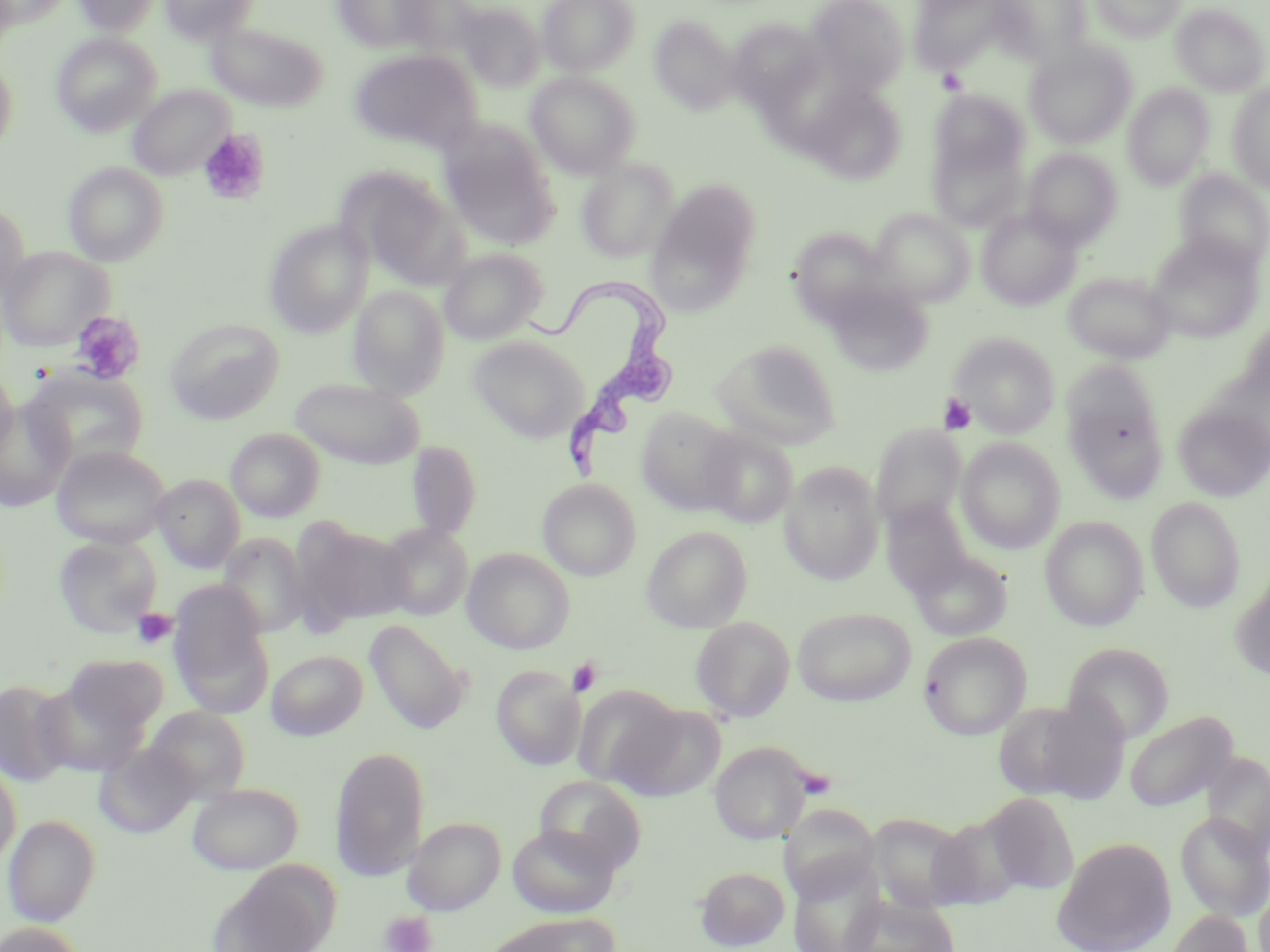
Approximate bounding boxes as [x1, y1, x2, y2] in pixels. Uninfected red blood cell locations: [73, 0, 162, 36], [158, 0, 261, 44], [333, 0, 436, 53], [537, 0, 640, 75], [805, 0, 909, 95], [909, 0, 1009, 73], [987, 0, 1092, 63], [1090, 0, 1185, 42], [393, 1, 481, 56], [454, 2, 547, 91], [1171, 3, 1269, 96], [649, 15, 739, 114], [728, 19, 828, 111], [206, 22, 328, 112], [52, 32, 161, 136], [1024, 41, 1137, 148], [349, 49, 482, 155], [0, 54, 18, 157], [526, 72, 640, 178], [805, 82, 906, 184], [1228, 83, 1270, 192], [1122, 84, 1214, 190], [127, 85, 234, 181], [929, 88, 1030, 189], [928, 126, 1028, 233], [440, 127, 556, 245], [1022, 148, 1122, 247], [576, 160, 678, 262], [63, 162, 168, 266], [340, 167, 469, 286], [1174, 170, 1270, 270], [651, 180, 761, 293], [0, 201, 29, 308], [977, 207, 1082, 310], [871, 208, 974, 306], [264, 220, 373, 338], [789, 227, 893, 323], [1147, 233, 1264, 343], [0, 246, 112, 351], [439, 248, 548, 345], [1063, 271, 1175, 363], [824, 281, 934, 376], [348, 287, 448, 398], [165, 318, 285, 424], [1237, 318, 1270, 415], [950, 332, 1060, 437], [466, 335, 591, 442], [712, 339, 841, 448], [1061, 361, 1169, 502], [0, 364, 18, 460], [24, 367, 150, 470], [290, 378, 425, 469], [0, 400, 73, 512], [1173, 404, 1270, 501], [636, 407, 739, 515], [870, 425, 967, 531], [697, 426, 798, 527], [225, 427, 326, 522], [957, 438, 1065, 553], [405, 439, 482, 541], [50, 444, 171, 548], [780, 462, 884, 585], [151, 474, 245, 573], [537, 478, 640, 581], [1146, 496, 1246, 612], [881, 498, 977, 597], [1040, 516, 1147, 632], [295, 519, 411, 628], [377, 523, 473, 621], [641, 526, 752, 633], [217, 533, 310, 638], [53, 534, 162, 637], [462, 548, 575, 654], [910, 550, 1013, 642], [1232, 576, 1270, 683], [168, 583, 273, 716], [792, 606, 916, 706], [690, 616, 796, 722], [365, 619, 471, 735], [918, 631, 1032, 739], [1063, 642, 1175, 743], [266, 649, 367, 740], [63, 654, 169, 735], [491, 665, 585, 771], [0, 679, 74, 787], [33, 679, 152, 776], [574, 685, 686, 791], [993, 697, 1122, 803], [146, 706, 251, 800], [1124, 710, 1237, 812], [709, 741, 813, 845], [94, 742, 199, 839], [330, 746, 430, 881], [0, 759, 21, 869], [535, 775, 646, 873], [187, 782, 304, 874], [983, 792, 1079, 895], [779, 803, 879, 904], [1175, 812, 1270, 921], [929, 813, 1025, 911], [2, 814, 101, 926], [867, 814, 972, 912], [402, 816, 505, 915], [507, 824, 621, 918], [1052, 836, 1177, 952], [787, 861, 884, 952], [695, 866, 789, 950], [207, 868, 333, 952], [1255, 882, 1270, 952], [842, 895, 961, 952], [1165, 910, 1255, 952], [487, 914, 616, 952], [0, 922, 87, 952]. Platelet locations: [937, 68, 967, 95], [198, 129, 269, 206], [69, 310, 145, 385], [938, 392, 976, 434], [131, 607, 178, 649], [567, 658, 602, 696], [794, 766, 837, 802], [379, 911, 436, 952]. Trypanosoma brucei locations: [523, 276, 680, 484]. Slide-level diagnosis: Trypanosoma brucei. Light microscopy. Captured at 1000x magnification. One field of a larger specimen. May-Grünwald-Giemsa-stained preparation. Thin blood film. Image is 1270×952 pixels.